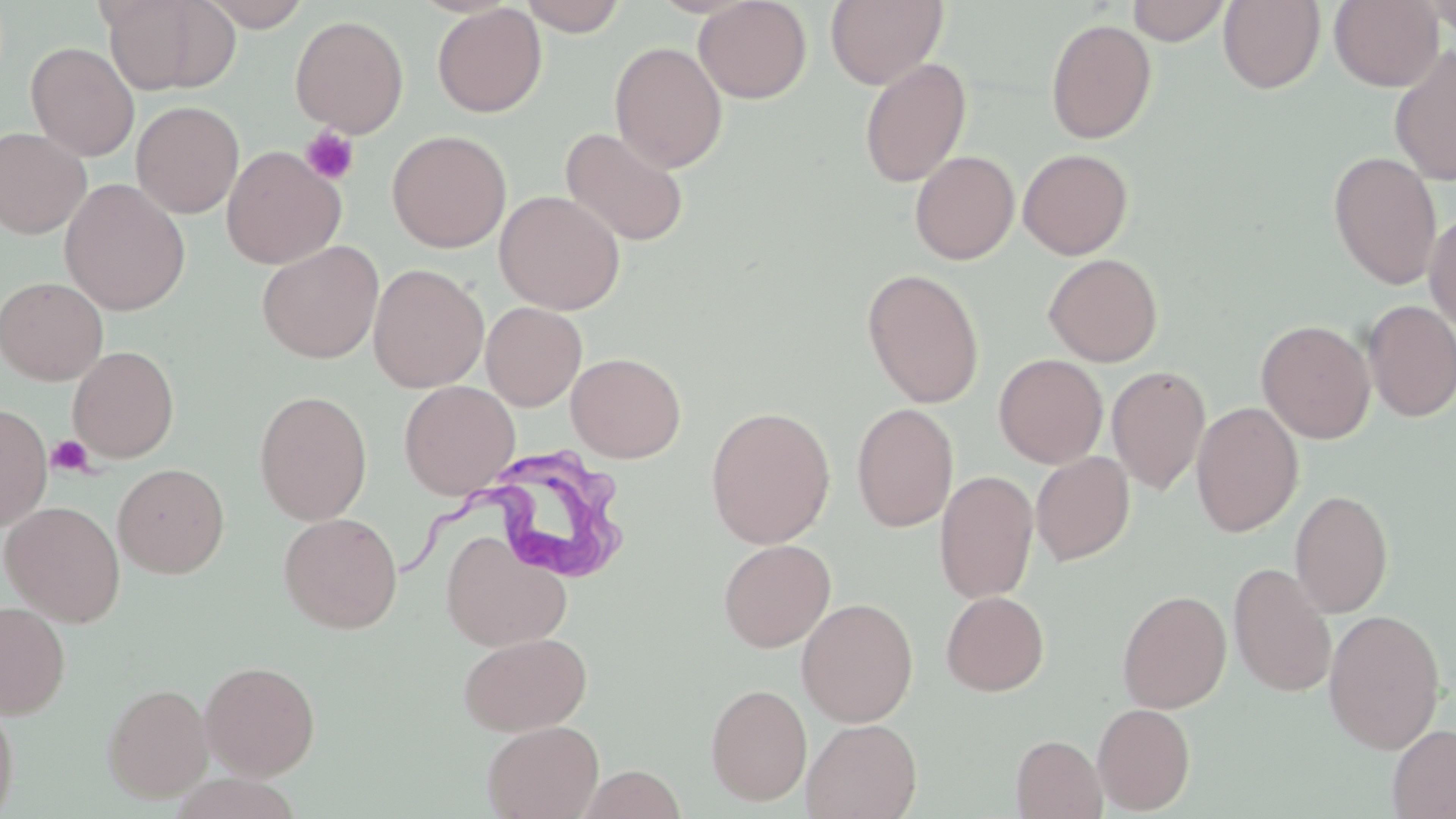
Summary:
  - Coordinate format: approximate bounding boxes as (x1, y1, x2, y2) in pixels
  - Trypanosoma brucei locations: (401, 442, 621, 589)
  - Uninfected red blood cell locations: (99, 0, 240, 96), (199, 0, 312, 30), (518, 0, 629, 36), (693, 0, 812, 103), (825, 0, 948, 89), (1127, 0, 1231, 46), (1329, 0, 1444, 90), (1422, 0, 1456, 40), (1219, 1, 1325, 93), (432, 3, 547, 118), (290, 14, 409, 138), (1045, 18, 1157, 144), (25, 41, 139, 161), (609, 41, 727, 172), (1389, 44, 1456, 187), (858, 58, 972, 188), (131, 100, 245, 218), (560, 126, 689, 247), (0, 128, 91, 239), (386, 130, 512, 253), (222, 145, 346, 269), (1018, 148, 1134, 259), (909, 150, 1020, 265), (1328, 151, 1443, 291), (59, 178, 191, 315), (494, 190, 626, 314), (1424, 206, 1456, 334), (256, 240, 384, 364), (1043, 253, 1164, 367), (368, 263, 489, 393), (861, 269, 985, 408), (0, 276, 108, 385), (1361, 299, 1456, 422), (481, 302, 587, 411), (1257, 319, 1376, 444), (67, 345, 179, 463), (566, 351, 686, 463), (993, 354, 1108, 468), (1107, 365, 1210, 495), (399, 380, 521, 500), (254, 390, 373, 526), (0, 402, 52, 530), (851, 402, 959, 532), (1191, 402, 1304, 537), (704, 406, 836, 549), (1031, 451, 1135, 566), (113, 463, 229, 578), (934, 469, 1039, 604), (1290, 489, 1393, 618), (1, 500, 126, 627), (278, 512, 403, 634), (441, 533, 572, 651), (718, 538, 836, 652), (1228, 561, 1337, 697), (1117, 589, 1231, 713), (941, 591, 1049, 696), (796, 598, 919, 727), (0, 601, 70, 719), (1323, 609, 1445, 754), (458, 631, 592, 736), (199, 660, 320, 779), (102, 682, 213, 802), (705, 682, 813, 806), (0, 695, 20, 819), (1093, 703, 1195, 814), (801, 717, 922, 819), (482, 719, 604, 819), (1387, 724, 1456, 818), (1011, 734, 1107, 819), (577, 765, 687, 819)
  - Platelet locations: (300, 126, 360, 186), (47, 434, 95, 477)
  - Slide-level diagnosis: Trypanosoma brucei
  - Stain: May-Grünwald-Giemsa
  - Modality: optical microscopy
  - Preparation: thin blood smear
  - Field of view: one of a larger specimen
  - Magnification: 1000x
  - Image size: 1456×819 pixels